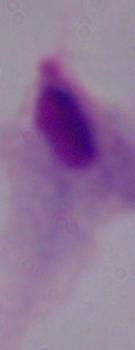

Photomicrograph. Captured at 1000x magnification. A trichomonad is seen.